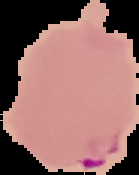
Result: Plasmodium parasites detected. Image is 139×175 pixels. From a thin blood smear. Segmented cell region on a black background.